Locate every blood parasite and identify its species.
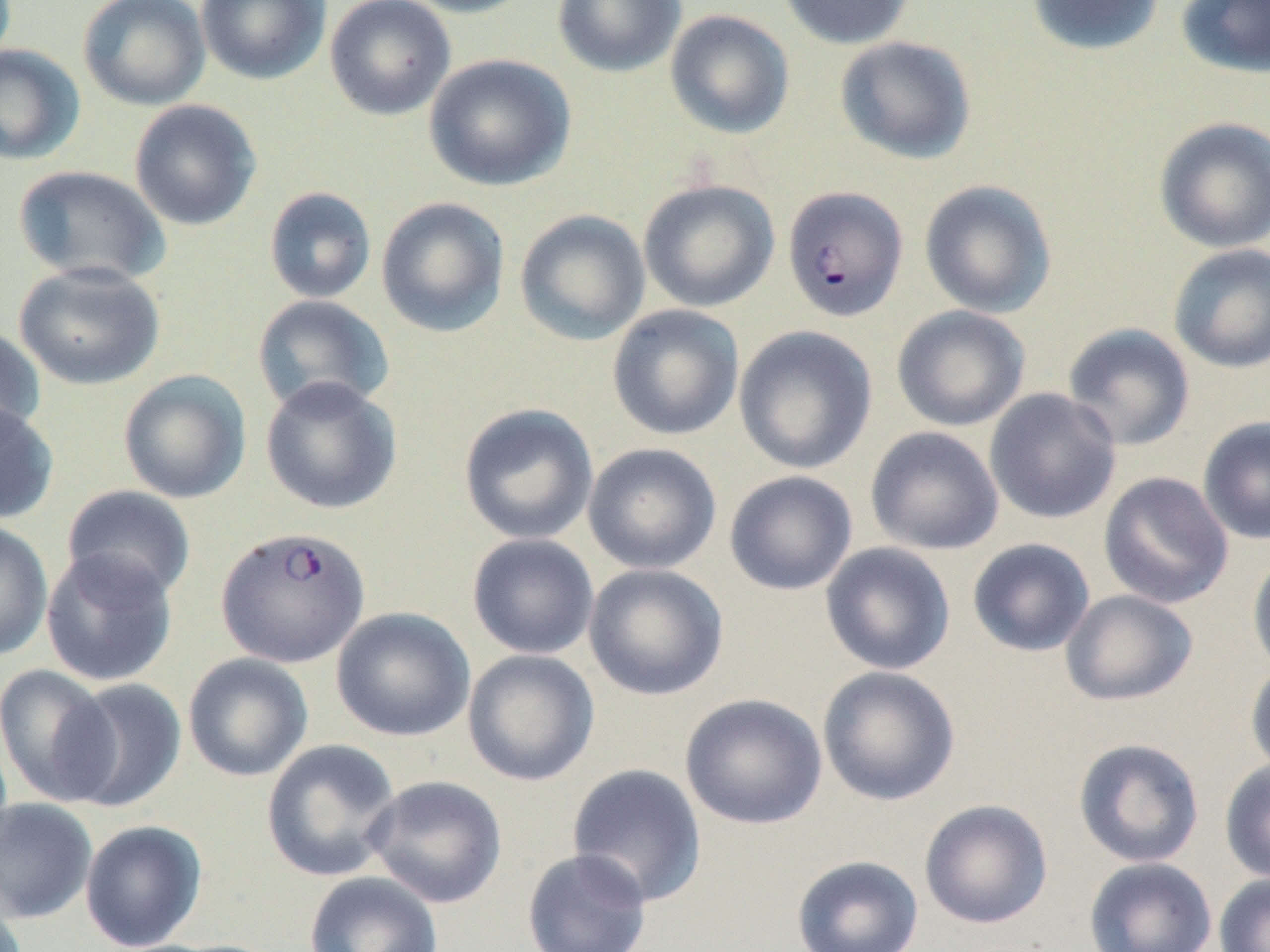

Approximate bounding boxes as (x1, y1, x2, y2) in pixels.
Plasmodium falciparum-infected red blood cells: (785, 184, 911, 320), (216, 526, 370, 668).
No Plasmodium ovale, Plasmodium malariae, Plasmodium vivax, Babesia divergens, or Trypanosoma brucei observed.

slide-level diagnosis = Plasmodium falciparum
image size = 1270×952 pixels
magnification = 1000x
preparation = thin blood smear
stain = May-Grünwald-Giemsa
modality = optical microscopy
uninfected red blood cell locations = approximate bounding boxes as (x1, y1, x2, y2) in pixels: (78, 0, 211, 111), (195, 0, 331, 85), (324, 0, 457, 121), (397, 0, 538, 18), (552, 0, 687, 78), (776, 0, 915, 49), (1026, 0, 1165, 56), (1175, 0, 1270, 78), (665, 9, 795, 139), (835, 35, 977, 164), (0, 44, 85, 165), (423, 53, 576, 192), (129, 99, 262, 231), (1154, 117, 1270, 254), (12, 165, 171, 287), (638, 178, 780, 313), (919, 180, 1057, 318), (263, 186, 377, 304), (376, 197, 510, 337), (514, 209, 650, 346), (1167, 243, 1270, 374), (14, 261, 165, 390), (252, 294, 394, 415), (607, 304, 745, 441), (891, 305, 1031, 432), (1062, 322, 1195, 452), (0, 325, 46, 444), (733, 325, 878, 474), (118, 369, 252, 504), (259, 376, 402, 515), (984, 388, 1122, 524), (0, 401, 59, 525), (458, 402, 599, 545), (1197, 415, 1270, 546), (865, 426, 1004, 555), (583, 443, 722, 574), (724, 470, 858, 596), (1098, 471, 1234, 609), (60, 485, 197, 602), (0, 520, 54, 662), (467, 533, 599, 660), (967, 537, 1095, 657), (820, 541, 956, 675), (40, 547, 178, 687), (1247, 552, 1270, 678), (584, 563, 729, 701), (1060, 590, 1199, 706), (331, 607, 475, 742), (462, 649, 600, 787), (183, 653, 314, 782), (1245, 660, 1270, 779), (0, 664, 119, 806), (817, 665, 961, 806), (60, 677, 187, 812), (680, 693, 827, 830), (261, 738, 402, 882), (1073, 738, 1205, 868), (1219, 758, 1270, 884), (566, 763, 708, 908), (363, 775, 507, 908), (0, 797, 99, 923), (919, 799, 1053, 929), (79, 819, 208, 951), (521, 847, 653, 952), (791, 855, 924, 952), (1084, 857, 1217, 952), (303, 871, 443, 952), (1214, 873, 1270, 952)
field of view = one of a larger specimen